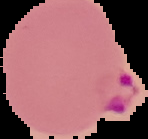
Summary:
  - Preparation: thin blood smear
  - Malaria status: parasitized
  - Image type: segmented cell region on a black background
  - Image size: 148×139 pixels